Look for Plasmodium parasites.
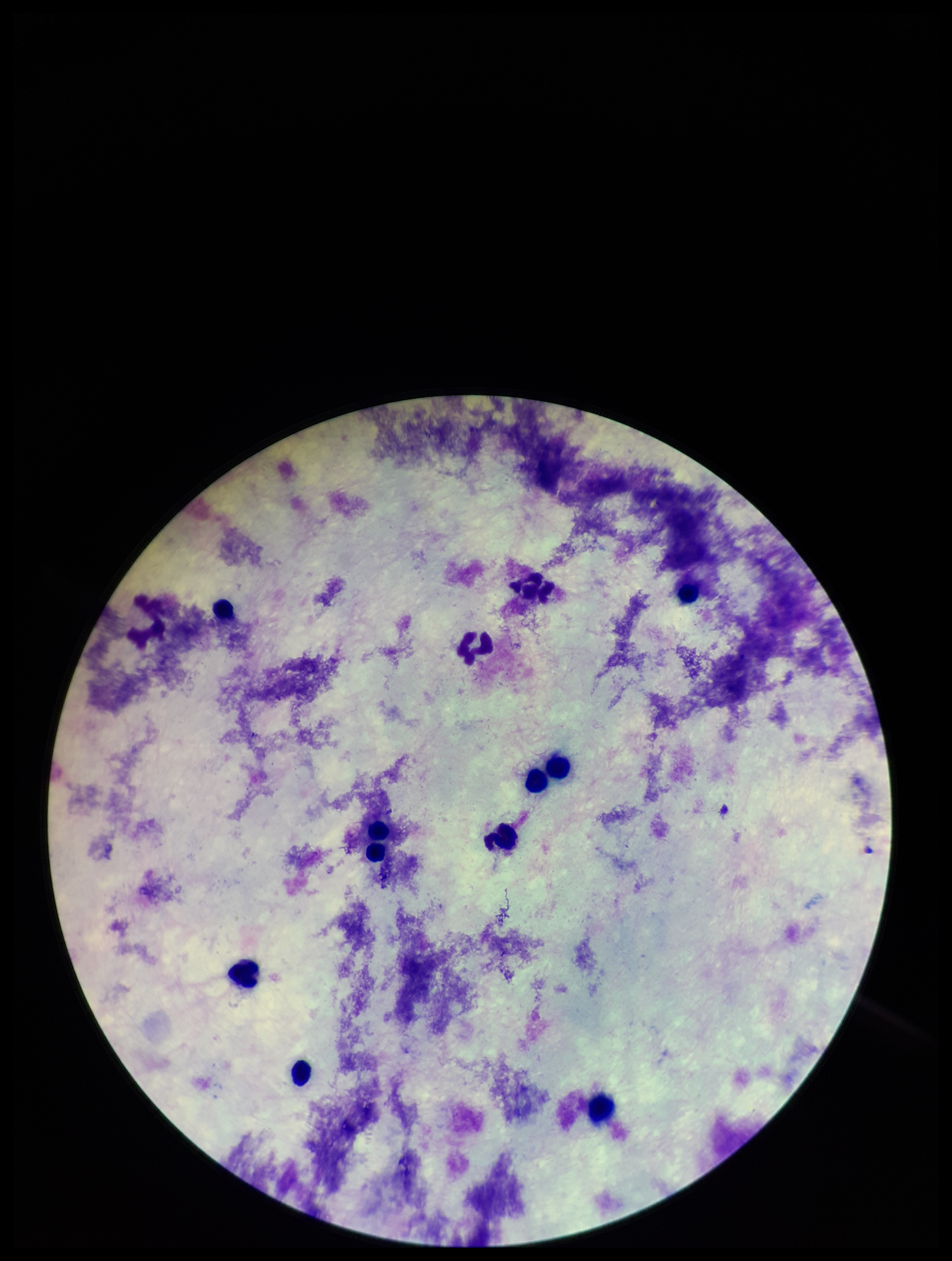
None seen.

Summary:
  - Preparation: thick
  - Capture: smartphone photograph through the microscope eyepiece
  - Field of view: single
  - Leukocyte count: 11
  - Image size: 952×1261 pixels
  - Parasite count: 0
  - Stain: Giemsa
  - Patient malaria status: negative